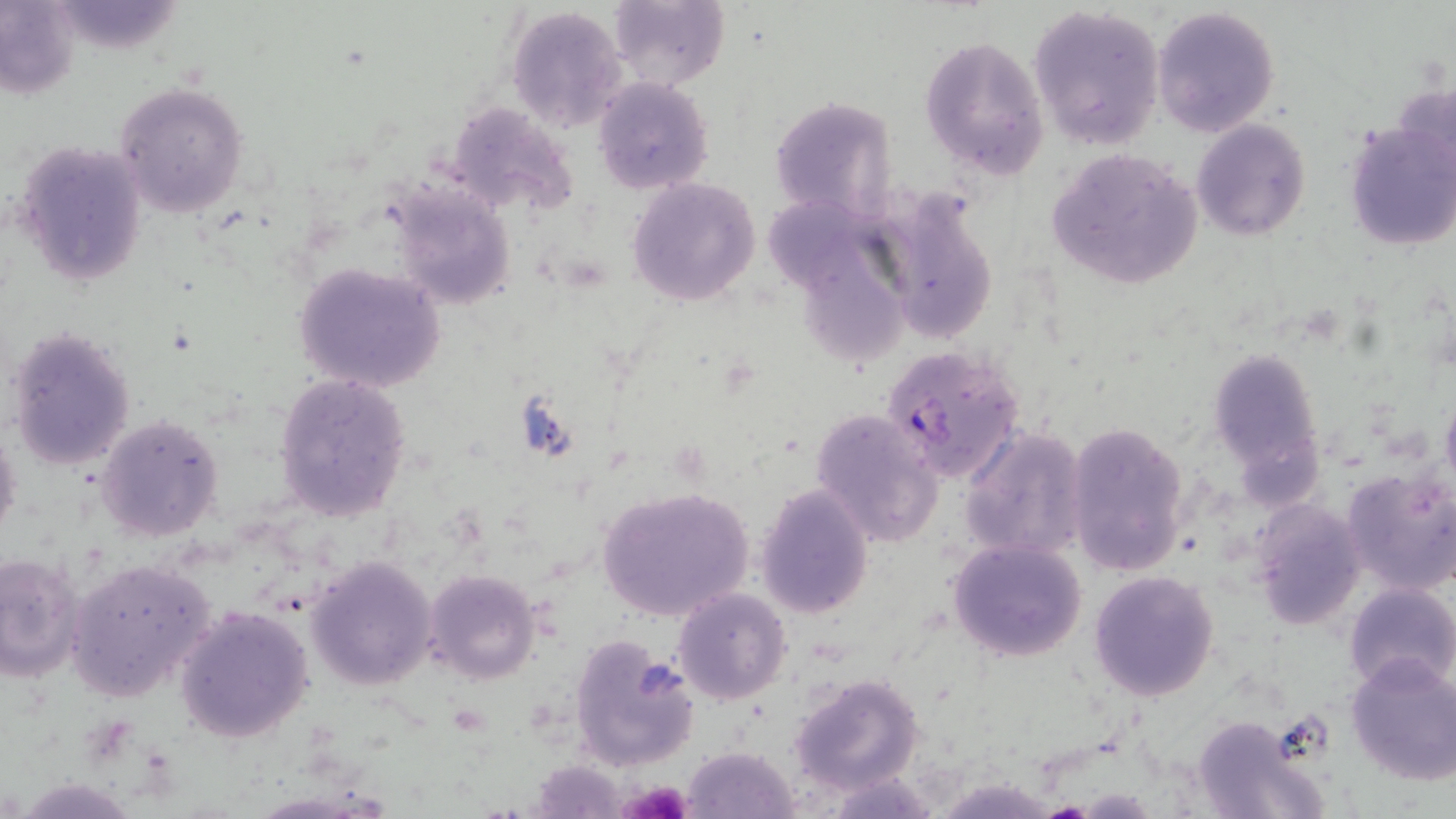

Summary:
  - Coordinate format: approximate bounding boxes as [x1, y1, x2, y2] in pixels
  - Plasmodium falciparum-infected red blood cell locations: [881, 345, 1026, 484]
  - Platelet locations: [621, 779, 693, 819]
  - Uninfected red blood cell locations: [607, 0, 729, 90], [0, 1, 82, 97], [62, 1, 186, 55], [1027, 4, 1166, 150], [1151, 4, 1280, 138], [507, 5, 628, 133], [921, 32, 1050, 182], [592, 77, 713, 194], [114, 82, 251, 217], [769, 95, 898, 223], [445, 102, 579, 219], [1345, 118, 1456, 252], [1191, 119, 1311, 239], [14, 139, 147, 289], [1046, 146, 1205, 292], [627, 177, 761, 305], [385, 179, 517, 311], [873, 187, 999, 348], [768, 198, 881, 291], [295, 261, 446, 394], [810, 267, 920, 366], [6, 324, 135, 474], [1210, 349, 1324, 482], [273, 374, 412, 521], [1439, 392, 1456, 491], [810, 409, 946, 547], [97, 414, 224, 541], [1064, 420, 1191, 578], [0, 424, 22, 551], [960, 425, 1090, 561], [1342, 465, 1456, 595], [755, 483, 874, 619], [595, 485, 755, 621], [1249, 499, 1367, 630], [948, 538, 1089, 662], [0, 551, 85, 681], [306, 556, 437, 690], [66, 557, 217, 702], [424, 568, 542, 684], [1089, 571, 1219, 700], [1344, 582, 1456, 694], [672, 587, 792, 704], [175, 606, 313, 743], [570, 635, 697, 770], [1344, 654, 1456, 785], [789, 673, 926, 796], [1190, 713, 1331, 819], [683, 745, 798, 817]
  - Slide-level diagnosis: Plasmodium falciparum
  - Preparation: thin blood smear
  - Image size: 1456×819 pixels
  - Stain: May-Grünwald-Giemsa
  - Modality: optical microscopy
  - Magnification: 1000x
  - Field of view: one of a larger specimen